Classify this cell by malaria status.
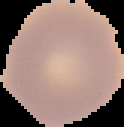

Uninfected.

Summary:
  - Image type: segmented cell region with the area outside set to black
  - Image size: 124×127 pixels
  - Preparation: thin blood smear